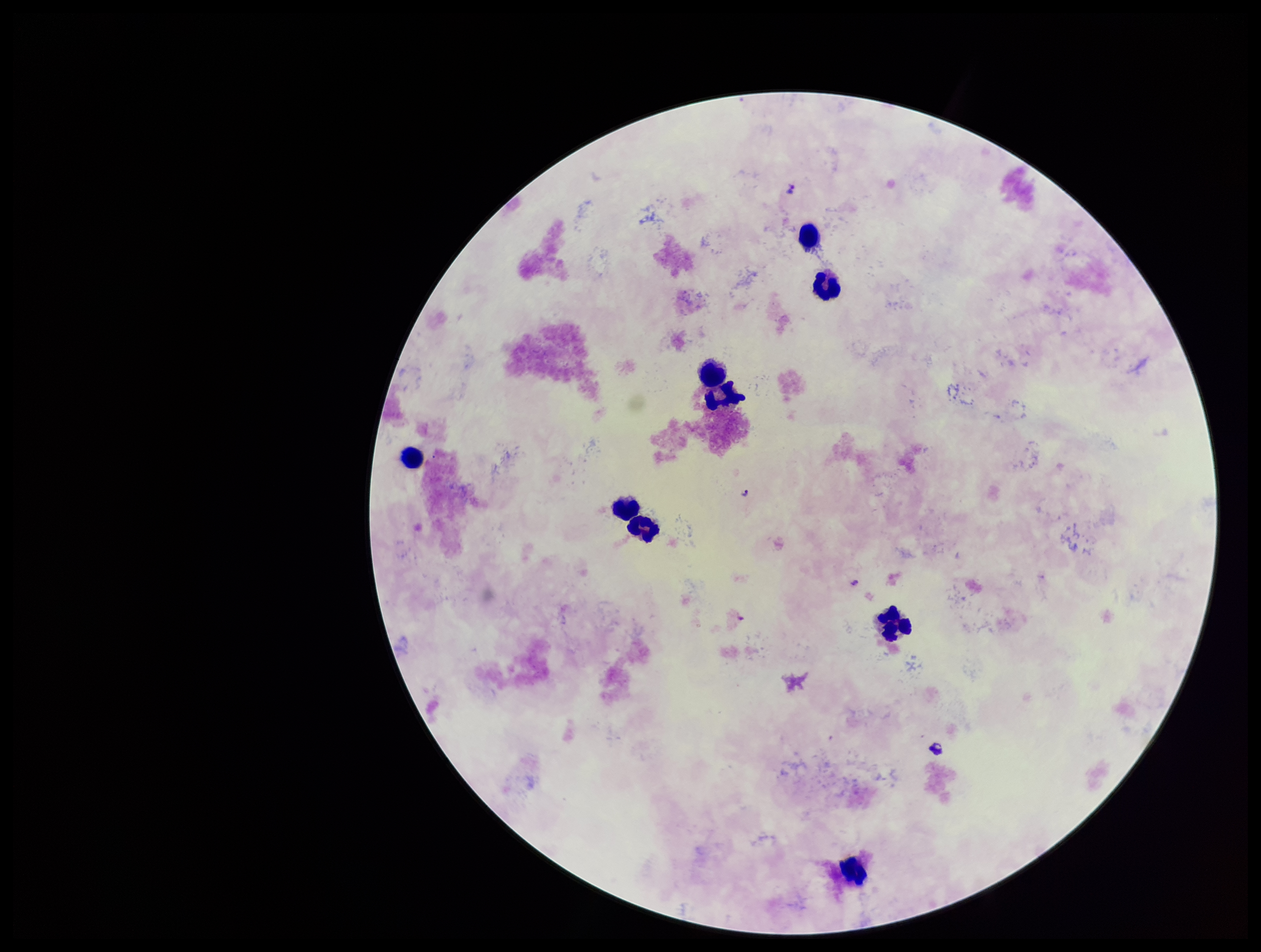

{
  "capture": "smartphone photograph through the microscope eyepiece",
  "stain": "Giemsa",
  "species_reported_for_this_patient": "Plasmodium falciparum",
  "field_of_view": "single",
  "preparation": "thick smear",
  "image_size": "1261×952 pixels",
  "leukocyte_count": 9,
  "patient_malaria_status": "positive",
  "plasmodium_parasites": "seen",
  "parasite_count": 3
}